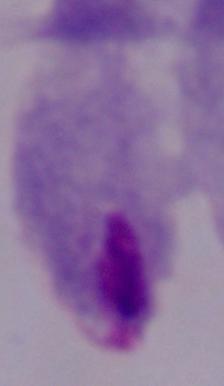
Summary:
  - Modality: micrograph
  - Identification: trichomonad
  - Magnification: 1000x